Classify this cell by malaria status.
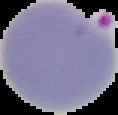

Parasitized.

Image is 118×115 pixels. The area outside the segmented cell region is set to black. From a thin blood film.